Outline each Plasmodium falciparum-infected red blood cell.
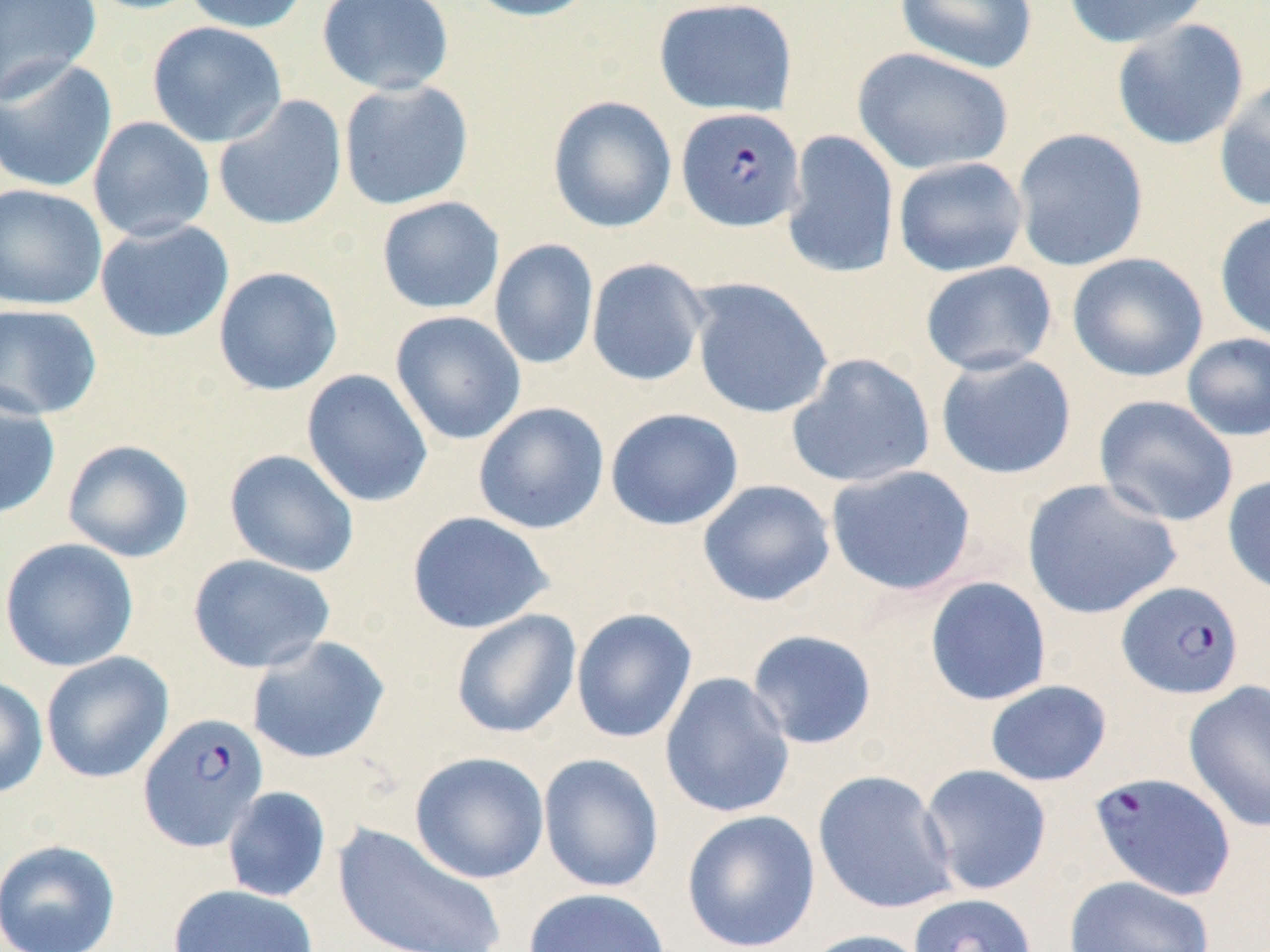
Approximate bounding boxes as [x1, y1, x2, y2] in pixels.
Plasmodium falciparum-infected red blood cells (subset): [676, 107, 805, 233], [1116, 581, 1244, 700], [138, 711, 269, 852], [1088, 771, 1237, 902].

Uninfected red blood cell locations (subset): [0, 0, 102, 103], [79, 0, 209, 15], [182, 0, 311, 34], [316, 0, 455, 95], [461, 0, 599, 22], [653, 0, 798, 117], [894, 0, 1039, 74], [1061, 0, 1214, 48], [1111, 19, 1250, 150], [147, 21, 288, 148], [852, 47, 1014, 176], [0, 56, 118, 194], [1213, 75, 1270, 212], [338, 79, 474, 210], [213, 94, 348, 231], [547, 95, 677, 233], [88, 116, 215, 242], [1012, 128, 1149, 272], [782, 130, 900, 280], [892, 157, 1028, 276], [0, 183, 108, 311], [376, 196, 505, 314], [1214, 209, 1270, 343], [94, 219, 234, 343], [489, 239, 599, 370], [1067, 252, 1209, 383], [586, 258, 710, 387], [919, 261, 1058, 378], [212, 266, 343, 396], [689, 278, 834, 420], [0, 303, 103, 420], [390, 310, 527, 445], [1181, 332, 1270, 442], [935, 352, 1077, 480], [786, 353, 936, 490], [301, 370, 434, 508], [0, 389, 61, 521], [1094, 395, 1239, 527], [473, 401, 609, 534], [605, 408, 743, 530], [62, 439, 194, 563], [224, 449, 360, 577], [825, 464, 977, 596], [1222, 474, 1270, 596], [1021, 478, 1183, 620], [697, 479, 836, 607], [406, 511, 554, 634], [1, 537, 139, 672], [187, 553, 335, 673], [924, 577, 1052, 706], [570, 608, 698, 743], [450, 609, 582, 739], [745, 629, 878, 750], [246, 636, 391, 765], [40, 651, 174, 783], [659, 672, 796, 819], [0, 676, 49, 798], [985, 680, 1112, 787], [1183, 680, 1270, 833], [410, 751, 550, 884], [537, 752, 665, 893], [918, 764, 1053, 896], [812, 769, 958, 915], [222, 786, 332, 903], [681, 809, 820, 951], [333, 823, 507, 952], [0, 839, 121, 951], [1063, 875, 1215, 952], [168, 884, 318, 952], [522, 887, 671, 952], [800, 929, 935, 952]. Slide-level diagnosis: Plasmodium falciparum. Image is 1270×952 pixels. Captured at 1000x magnification. Light microscopy. Thin blood smear. One field of a larger specimen. May-Grünwald-Giemsa-stained preparation.